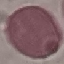 Result: no malaria parasites detected. Giemsa stain. Photographed with a smartphone camera at the microscope eyepiece. Thin blood film. Cell patch, automatically extracted from a larger field of view and resized to 64 × 64 pixels.